Describe the morphology of the red blood cells.
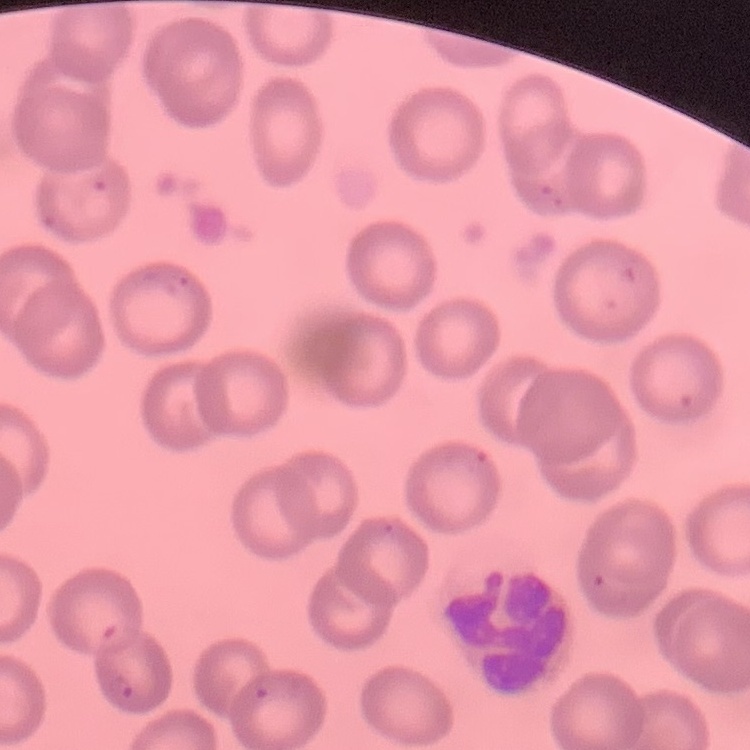
No rouleaux formation.

{
  "preparation": "thin peripheral smear",
  "stain": "Field's or Giemsa",
  "image_type": "square crop of a larger photomicrograph"
}